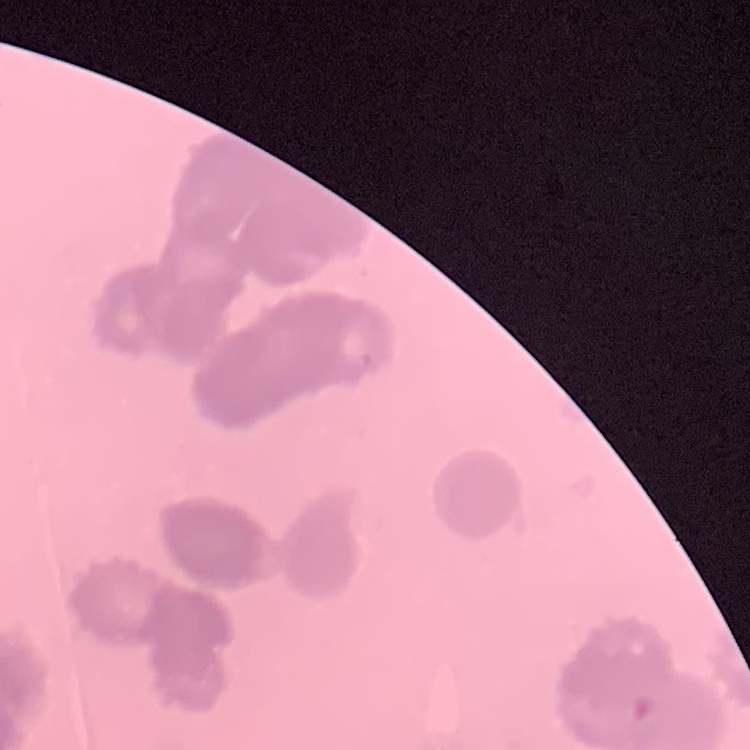

Summary:
  - Erythrocyte morphology: rouleaux formation
  - Image type: one tile cut from a larger photomicrograph
  - Stain: Field's or Giemsa
  - Preparation: thin blood smear